Assess this cell for malaria.
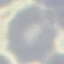
Uninfected.

capture = smartphone through the microscope eyepiece
image type = automatically extracted cell patch, resized to 64 × 64 pixels
preparation = thin smear
stain = Giemsa